Report the malaria status of this cell.
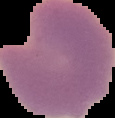

It is parasitized.

{
  "image_size": "115×118 pixels",
  "preparation": "thin blood film",
  "image_type": "segmented cell region on a black background"
}